Name the parasite shown.
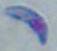
Toxoplasma gondii.

Micrograph. 1000x magnification.